Identify the parasite.
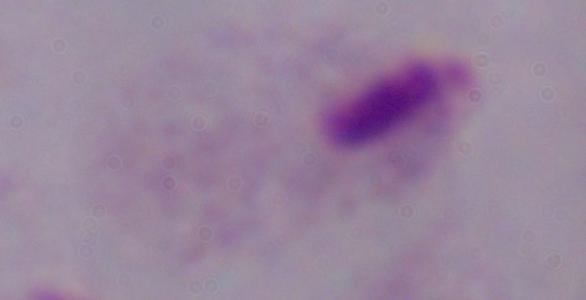
This is a trichomonad.

Photomicrograph. Captured at 1000x magnification.